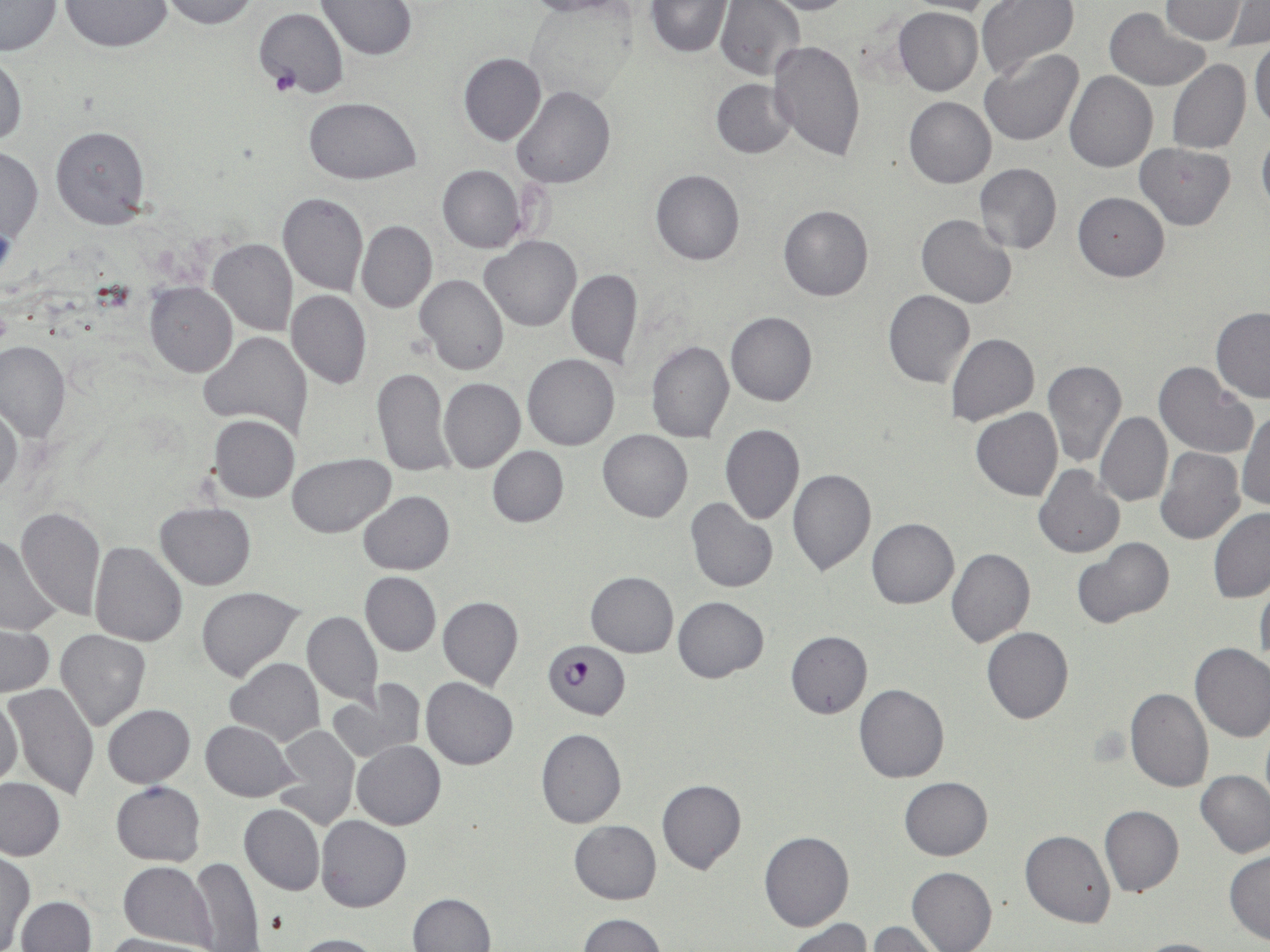

Summary:
  - Coordinate format: approximate bounding boxes as (x1,y1)-(x2,y2) corner pairs in pixels
  - Plasmodium falciparum-infected red blood cell locations: (544,641)-(630,718)
  - Uninfected red blood cell locations: (159,0)-(260,29), (317,0)-(418,60), (516,0)-(638,18), (760,0)-(862,14), (976,0)-(1078,80), (1161,0)-(1248,44), (645,1)-(733,56), (715,1)-(805,81), (906,1)-(1011,16), (0,2)-(62,56), (60,2)-(173,51), (1219,3)-(1269,49), (893,6)-(983,96), (252,7)-(348,98), (1104,8)-(1210,91), (1250,39)-(1270,129), (768,40)-(866,160), (979,48)-(1084,146), (1,51)-(26,150), (459,53)-(546,146), (1167,59)-(1251,155), (1063,70)-(1158,173), (710,78)-(797,158), (512,86)-(617,189), (305,96)-(420,183), (904,96)-(996,188), (49,126)-(150,228), (1257,129)-(1270,221), (1134,143)-(1236,230), (0,148)-(43,244), (974,163)-(1062,254), (437,165)-(526,253), (650,170)-(744,265), (277,191)-(368,295), (1072,192)-(1169,281), (778,205)-(874,302), (916,214)-(1018,308), (356,220)-(437,313), (481,236)-(581,331), (208,240)-(297,337), (566,268)-(643,369), (415,274)-(511,374), (146,284)-(237,377), (883,288)-(975,387), (286,289)-(371,389), (1210,307)-(1270,403), (725,310)-(818,406), (199,330)-(313,437), (946,334)-(1039,425), (645,340)-(734,443), (0,341)-(71,442), (523,353)-(619,450), (1043,359)-(1127,468), (1153,362)-(1257,460), (371,366)-(455,478), (438,378)-(525,472), (0,406)-(21,499), (972,408)-(1063,501), (1237,410)-(1269,512), (1095,411)-(1173,507), (209,414)-(299,502), (719,423)-(805,525), (598,429)-(693,522), (486,446)-(568,527), (1156,447)-(1245,545), (288,454)-(396,537), (1034,465)-(1125,558), (787,468)-(876,575), (357,491)-(455,574), (686,499)-(778,593), (155,502)-(257,589), (14,506)-(106,621), (1208,508)-(1270,603), (866,518)-(959,609), (0,535)-(61,636), (1073,538)-(1173,628), (89,541)-(187,647), (947,547)-(1035,647), (359,572)-(441,656), (585,572)-(678,657), (1255,583)-(1270,671), (197,586)-(304,682), (437,596)-(523,690), (672,596)-(769,682), (302,611)-(383,703), (0,626)-(54,697), (982,627)-(1074,724), (55,629)-(150,730), (785,631)-(872,718), (1189,642)-(1270,742), (226,658)-(324,747), (421,677)-(519,770), (328,683)-(421,765), (4,684)-(100,798), (854,684)-(950,784), (1125,687)-(1212,792), (0,695)-(24,789), (103,704)-(195,787), (201,721)-(298,801), (273,725)-(361,831), (535,728)-(626,829), (352,741)-(446,829), (1196,769)-(1270,859), (0,777)-(66,861), (899,777)-(993,860), (657,779)-(746,875), (111,781)-(206,865), (239,803)-(324,896), (1099,806)-(1183,898), (316,815)-(412,912), (569,820)-(661,904), (1019,830)-(1117,927), (759,831)-(854,932), (1225,850)-(1270,945), (1,851)-(34,950), (190,858)-(263,951), (119,861)-(218,949), (906,866)-(997,952), (408,892)-(496,952), (17,895)-(95,952), (578,913)-(666,951), (785,918)-(871,952), (866,922)-(947,952), (100,934)-(211,952), (291,934)-(386,952), (1128,938)-(1230,952)
  - Slide-level diagnosis: Plasmodium falciparum
  - Stain: May-Grünwald-Giemsa
  - Preparation: thin blood smear
  - Image size: 1270×952 pixels
  - Field of view: single
  - Magnification: 1000x
  - Modality: light microscopy